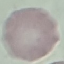
Result: negative for malaria parasites. Giemsa-stained preparation. Cell patch, automatically extracted from a larger field of view and resized to 64 × 64 pixels. Thin blood film. Photographed with a smartphone camera at the microscope eyepiece.